Describe the morphology of the erythrocytes.
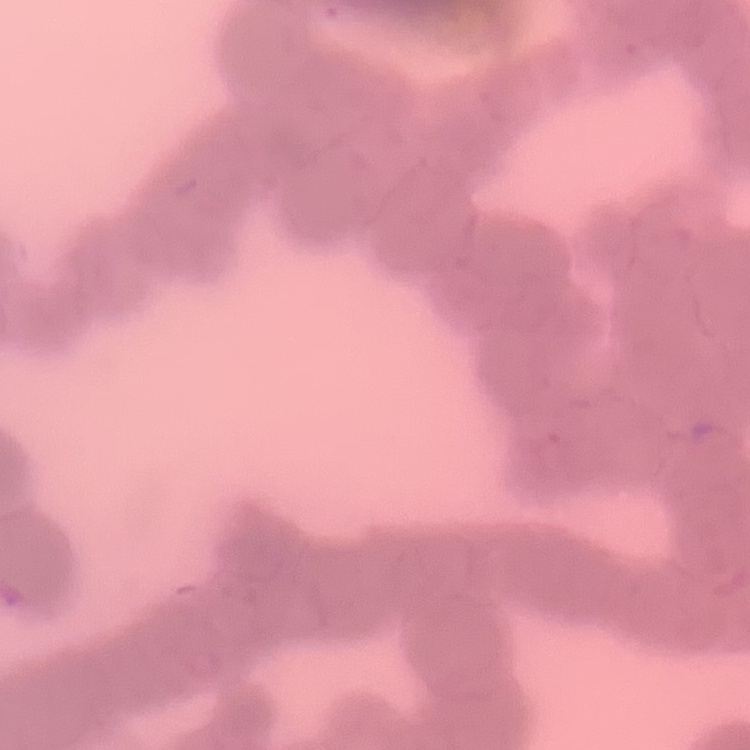
They show rouleaux formation.

{
  "image_type": "one tile cut from a larger photomicrograph",
  "stain": "Field's or Giemsa",
  "preparation": "thin peripheral smear"
}